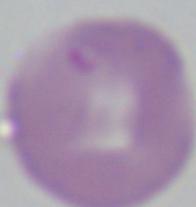
1000x magnification. Photomicrograph. A Babesia parasite is seen.